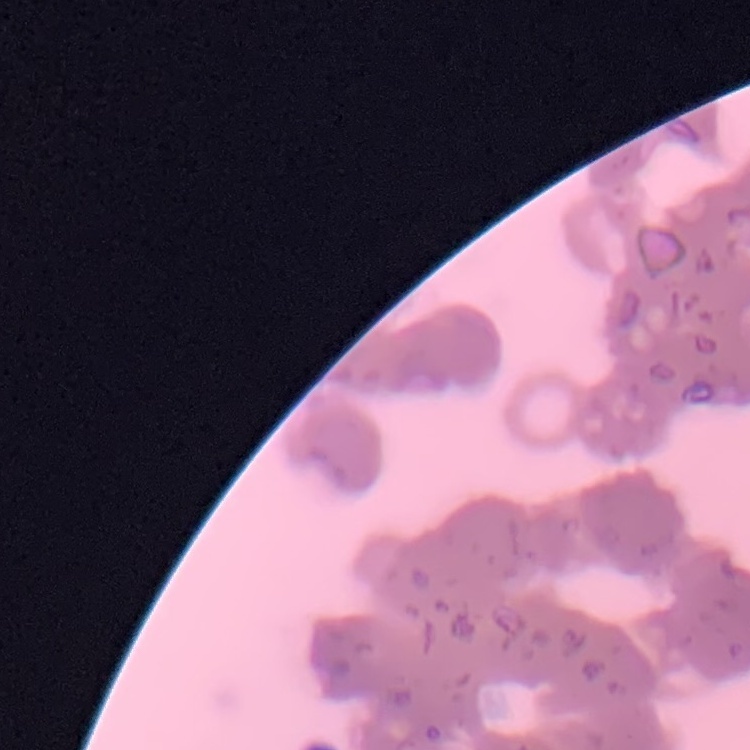

Summary:
  - Erythrocyte morphology: rouleaux formation
  - Stain: Field's or Giemsa
  - Preparation: thin blood film
  - Image type: one tile cut from a larger photomicrograph